Give the extent of all Plasmodium falciparum-infected red blood cells.
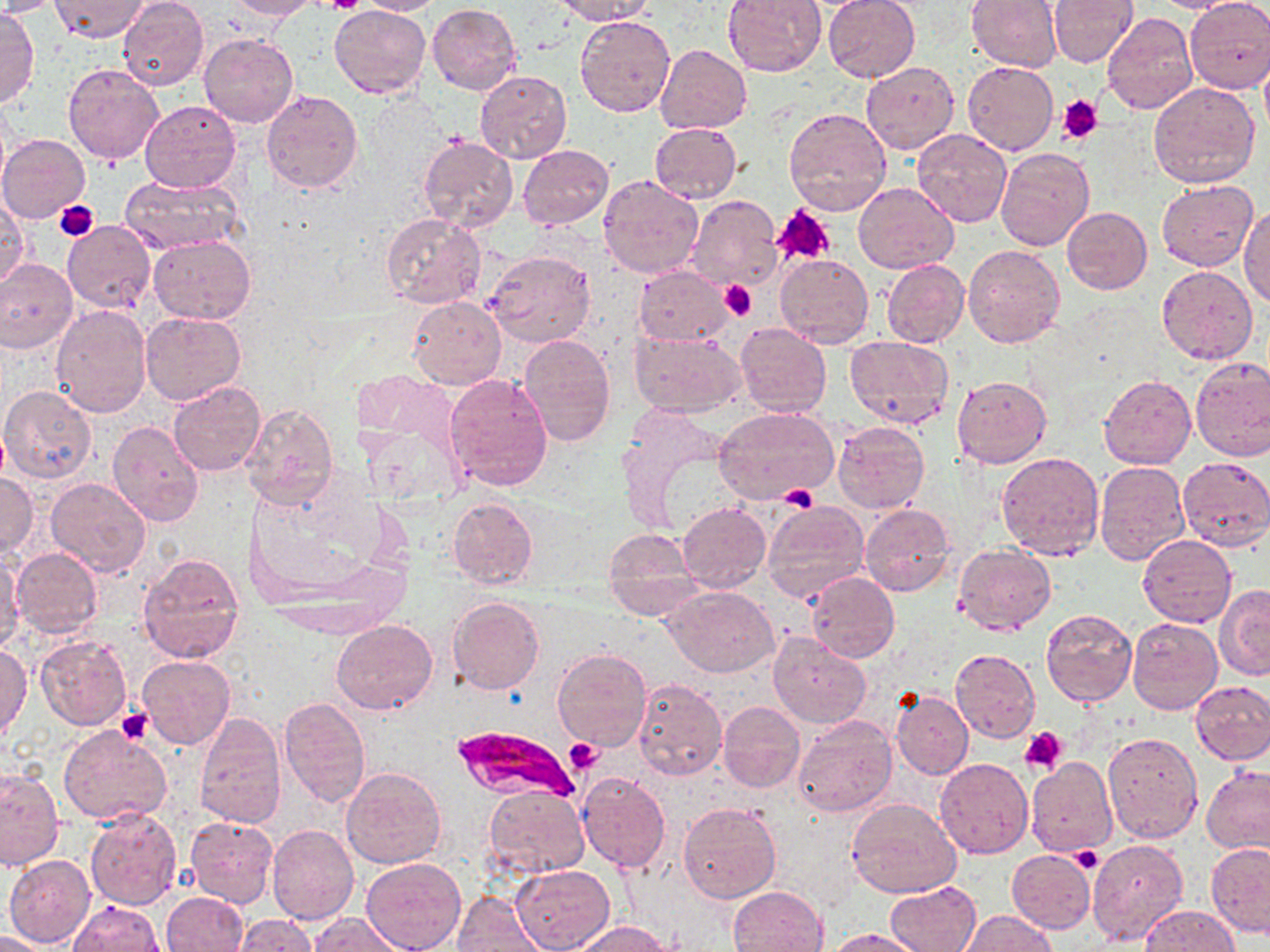

Approximate bounding boxes as (x1,y1)-(x2,y2) corner pairs in pixels.
Plasmodium falciparum-infected red blood cells: (450,724)-(578,806).

{
  "slide_level_diagnosis": "Plasmodium falciparum",
  "modality": "optical microscopy",
  "stain": "May-Grünwald-Giemsa",
  "magnification": "1000x",
  "uninfected_red_blood_cell_locations": "approximate bounding boxes as (x1,y1)-(x2,y2) corner pairs in pixels: (0,0)-(61,16), (50,0)-(150,41), (225,0)-(321,20), (354,0)-(446,15), (552,0)-(654,24), (722,0)-(826,76), (823,0)-(920,81), (1049,0)-(1137,66), (1148,0)-(1248,13), (1183,0)-(1270,94), (117,1)-(209,91), (965,1)-(1061,72), (428,4)-(521,94), (328,5)-(430,98), (1,6)-(38,108), (1101,13)-(1198,116), (576,16)-(675,119), (199,33)-(297,128), (656,43)-(752,134), (962,60)-(1058,155), (861,61)-(959,153), (63,64)-(164,166), (476,71)-(571,163), (1147,82)-(1260,189), (261,88)-(363,193), (141,100)-(240,192), (783,107)-(892,217), (649,122)-(741,203), (912,130)-(1012,228), (0,133)-(90,222), (419,135)-(518,231), (953,137)-(1062,241), (519,144)-(613,230), (994,146)-(1093,252), (121,174)-(246,253), (597,174)-(705,279), (1157,180)-(1256,271), (853,183)-(959,273), (684,195)-(783,291), (0,197)-(30,288), (1238,206)-(1269,307), (1060,207)-(1152,294), (382,213)-(487,309), (62,221)-(156,313), (149,236)-(255,325), (961,245)-(1064,349), (485,249)-(596,347), (775,254)-(873,347), (0,259)-(78,352), (882,259)-(969,349), (1156,265)-(1259,365), (634,266)-(734,345), (408,296)-(505,390), (51,304)-(151,417), (140,311)-(247,407), (734,323)-(832,417), (631,331)-(746,418), (518,335)-(616,445), (844,335)-(954,428), (1189,358)-(1270,461), (445,374)-(554,492), (1099,374)-(1195,470), (953,375)-(1052,468), (169,381)-(264,476), (0,386)-(98,483), (240,401)-(339,511), (715,406)-(839,506), (108,420)-(204,526), (833,421)-(929,513), (59,433)-(192,564), (996,452)-(1104,560), (1178,456)-(1270,551), (1095,460)-(1190,566), (0,473)-(38,558), (46,477)-(151,577), (446,498)-(537,589), (763,500)-(868,602), (677,502)-(771,591), (861,504)-(954,597), (601,530)-(700,617), (1138,534)-(1235,627), (954,545)-(1055,634), (12,547)-(105,638), (1,549)-(24,653), (137,552)-(245,663), (806,572)-(899,661), (1215,585)-(1269,680), (666,587)-(779,676), (447,596)-(544,695), (1042,608)-(1137,707), (1128,618)-(1222,714), (332,619)-(437,715), (768,633)-(870,728), (36,635)-(131,731), (0,642)-(31,742), (554,649)-(652,750), (951,650)-(1039,741), (137,655)-(236,750), (633,678)-(726,780), (1191,680)-(1270,764), (891,691)-(973,779), (279,698)-(371,807), (718,701)-(805,793), (194,713)-(287,829), (793,716)-(898,818), (58,725)-(172,825), (1102,731)-(1203,842), (1026,755)-(1119,856), (935,758)-(1033,858), (0,765)-(64,873), (1202,765)-(1270,854), (341,766)-(444,869), (578,772)-(670,874), (483,786)-(589,879), (848,798)-(960,899), (676,802)-(782,905), (85,808)-(182,911), (185,816)-(277,908), (267,825)-(359,926), (1087,840)-(1188,947), (1206,843)-(1270,938), (1067,845)-(1104,877), (1007,849)-(1096,934), (5,855)-(95,947), (360,858)-(466,952), (512,865)-(615,952), (886,881)-(979,952), (728,886)-(828,952), (163,891)-(248,952), (452,892)-(546,952), (68,901)-(165,952), (1137,905)-(1239,951), (960,911)-(1059,952), (309,913)-(404,952), (232,915)-(317,951), (572,921)-(670,952), (828,928)-(925,951), (0,931)-(53,951)",
  "platelet_locations": "approximate bounding boxes as (x1,y1)-(x2,y2) corner pairs in pixels: (322,0)-(366,15), (1059,94)-(1103,143), (55,199)-(97,240), (773,205)-(835,266), (720,280)-(757,320), (779,485)-(819,511), (117,707)-(153,745), (1019,727)-(1067,774), (563,739)-(602,773), (1072,849)-(1102,872)",
  "preparation": "thin blood film",
  "image_size": "1270×952 pixels",
  "field_of_view": "one of a larger specimen"
}